State which parasite is depicted.
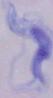
A trypanosome.

Summary:
  - Modality: micrograph
  - Magnification: 1000x